Point out each Plasmodium parasite.
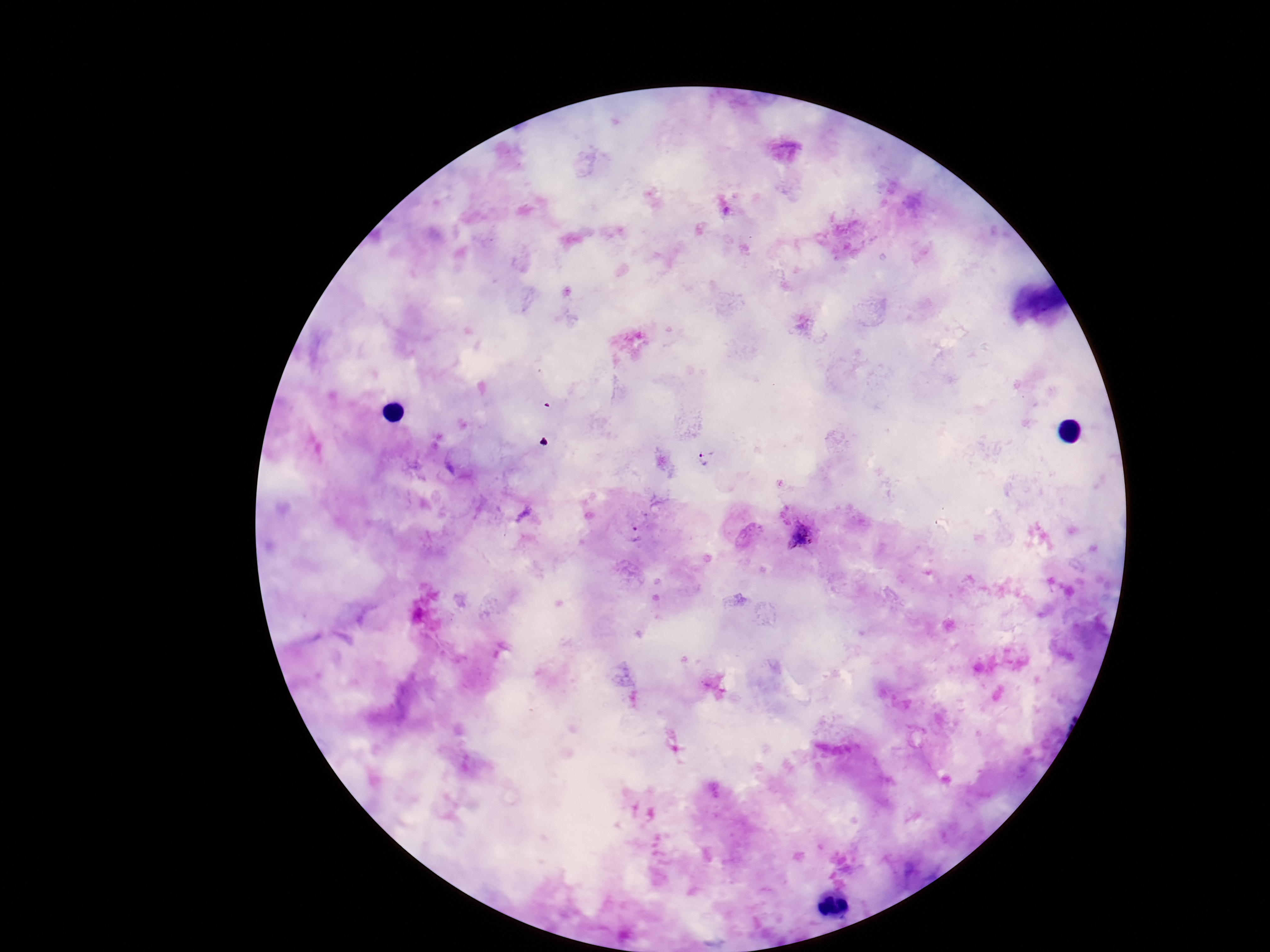
Approximate centers as {x, y} in pixels.
Plasmodium parasites: {704, 457}, {801, 535}, {636, 536}.

Summary:
  - Field of view: one from this slide
  - Image size: 1270×952 pixels
  - Magnification: 100x
  - Preparation: thick blood film
  - Capture: smartphone camera through the microscope eyepiece
  - Stain: Giemsa
  - Patient malaria status: positive